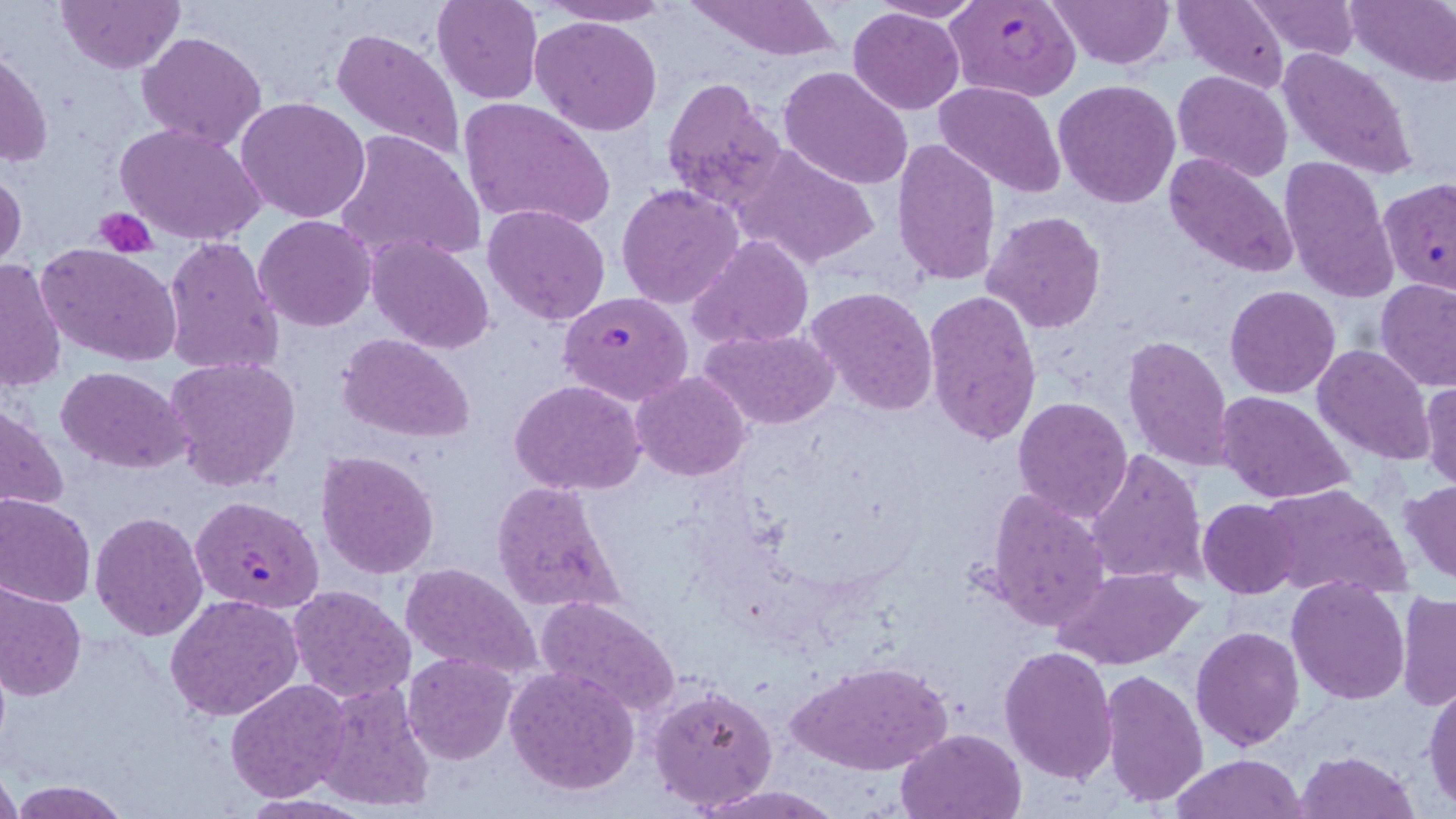

slide-level diagnosis = Plasmodium falciparum
preparation = thin blood film
modality = light microscopy
magnification = 1000x
field of view = single
Plasmodium falciparum-infected red blood cell locations = approximate bounding boxes as [x1, y1, x2, y2] in pixels: [945, 0, 1083, 102], [1378, 177, 1456, 295], [559, 291, 694, 406], [190, 495, 325, 614]
uninfected red blood cell locations = approximate bounding boxes as [x1, y1, x2, y2] in pixels: [57, 0, 184, 73], [431, 0, 542, 104], [539, 0, 677, 26], [866, 0, 986, 24], [1047, 0, 1173, 68], [1173, 0, 1290, 92], [1345, 0, 1456, 85], [685, 1, 845, 62], [1245, 1, 1361, 62], [847, 6, 964, 114], [530, 16, 661, 136], [330, 26, 465, 164], [138, 31, 267, 151], [1278, 47, 1418, 181], [1, 48, 52, 168], [778, 65, 913, 190], [1172, 71, 1293, 184], [661, 76, 786, 212], [1054, 79, 1180, 208], [936, 80, 1065, 200], [236, 97, 371, 225], [458, 97, 616, 233], [116, 123, 267, 247], [333, 131, 485, 268], [890, 136, 1003, 288], [734, 141, 882, 270], [1165, 153, 1299, 279], [1278, 154, 1399, 302], [0, 169, 27, 275], [615, 183, 745, 312], [483, 203, 611, 326], [981, 210, 1108, 334], [253, 215, 378, 331], [688, 235, 814, 350], [162, 236, 285, 379], [366, 236, 495, 354], [37, 243, 183, 368], [0, 259, 68, 394], [1376, 278, 1455, 391], [803, 285, 939, 415], [1225, 285, 1342, 399], [921, 288, 1042, 446], [700, 326, 841, 430], [338, 333, 477, 442], [1122, 335, 1234, 473], [1312, 344, 1437, 464], [164, 356, 302, 489], [57, 366, 188, 473], [630, 371, 751, 482], [1420, 380, 1456, 492], [510, 381, 645, 496], [1214, 391, 1355, 506], [1012, 395, 1134, 523], [0, 402, 69, 520], [1245, 417, 1398, 569], [1085, 448, 1209, 588], [315, 449, 440, 579], [491, 479, 625, 613], [1401, 481, 1456, 585], [1259, 483, 1409, 600], [984, 488, 1112, 633], [0, 495, 96, 608], [1197, 499, 1301, 598], [90, 512, 207, 640], [399, 562, 542, 682], [1054, 567, 1201, 671], [1286, 578, 1411, 703], [0, 583, 86, 702], [287, 583, 416, 704], [1396, 592, 1456, 710], [166, 593, 304, 722], [536, 597, 679, 716], [1191, 627, 1304, 750], [1000, 644, 1119, 786], [403, 651, 518, 764], [787, 660, 952, 777], [505, 666, 639, 795], [1100, 669, 1208, 809], [1422, 675, 1456, 810], [226, 678, 350, 802], [315, 681, 435, 812], [649, 683, 779, 813], [896, 728, 1024, 818], [1296, 749, 1420, 819], [1173, 753, 1306, 819], [0, 767, 21, 818], [10, 780, 132, 818], [693, 784, 837, 818], [240, 794, 370, 818]
platelet locations = approximate bounding boxes as [x1, y1, x2, y2] in pixels: [94, 206, 159, 256]
image size = 1456×819 pixels
stain = May-Grünwald-Giemsa